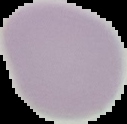

Summary:
  - Preparation: thin blood film
  - Image size: 127×124 pixels
  - Result: no Plasmodium parasites detected
  - Image type: segmented cell region on a black background